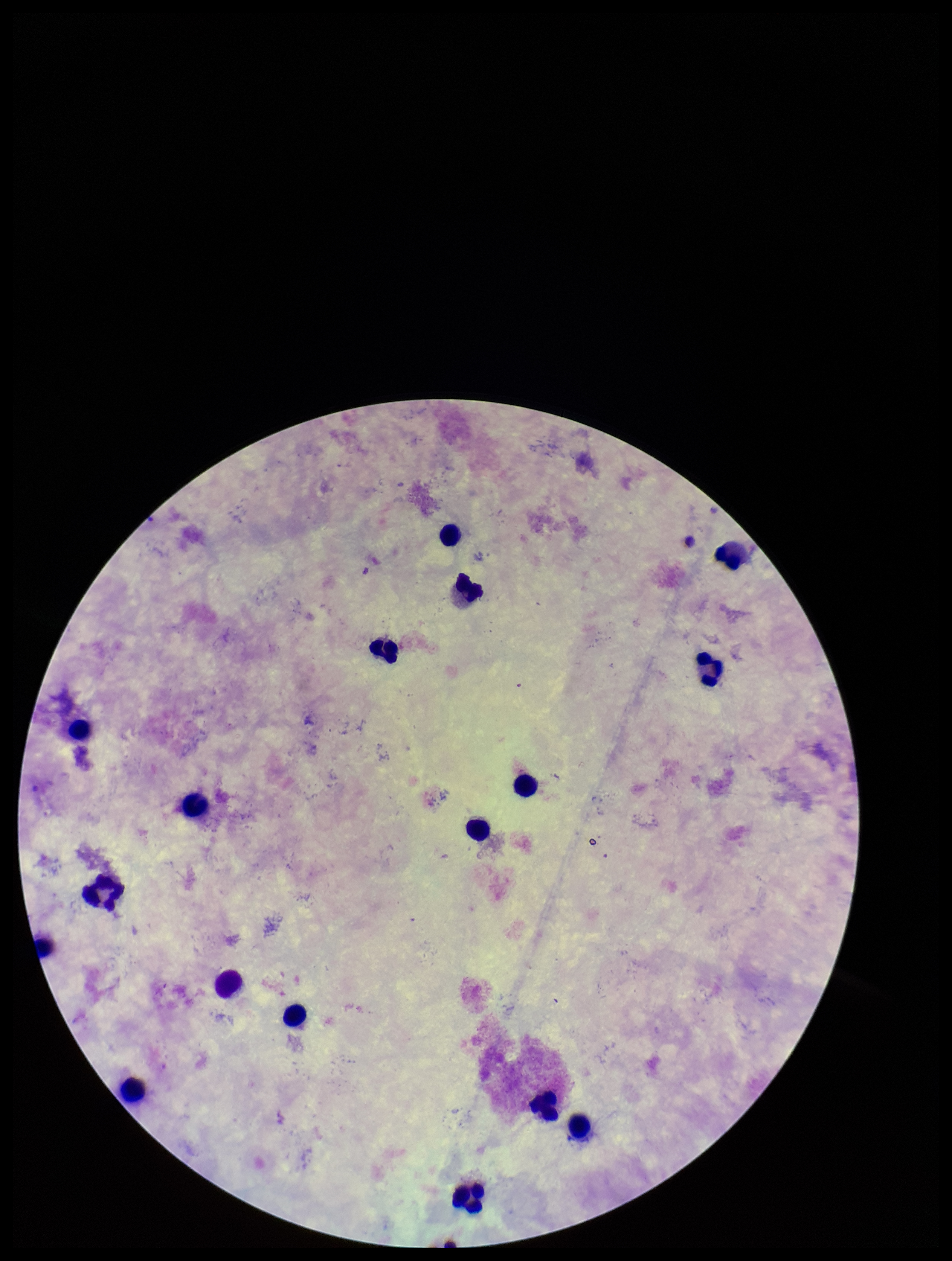
Summary:
  - Capture: smartphone photograph through the microscope eyepiece
  - Preparation: thick smear
  - Parasite count: 0
  - Plasmodium parasites: none identified
  - Leukocyte count: 17
  - Stain: Giemsa
  - Image size: 952×1261 pixels
  - Patient malaria status: negative
  - Field of view: one from this slide